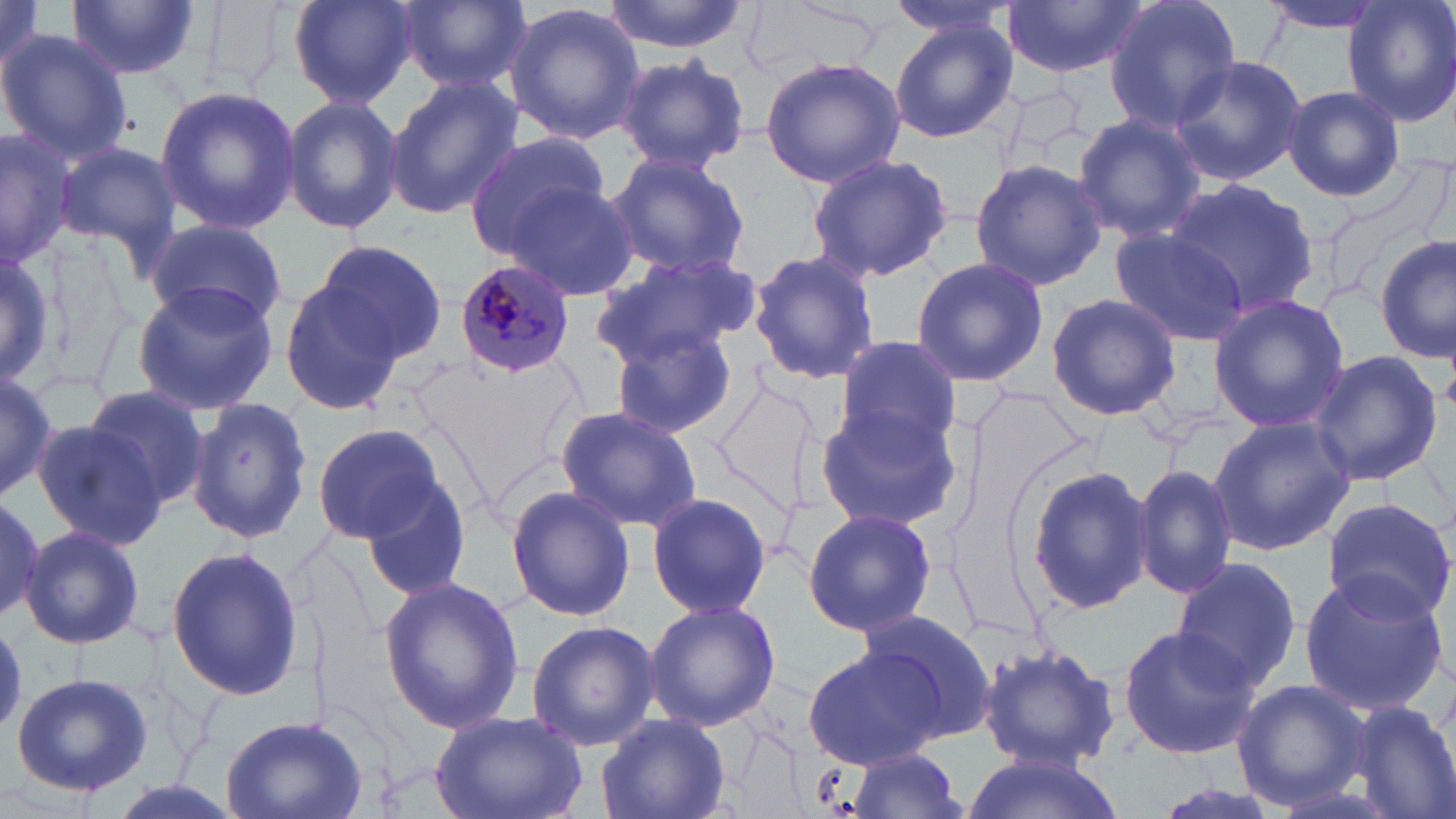 Approximate bounding boxes as named x1/y1/x2/y2 corners in pixels. Uninfected red blood cell locations: (x1=287, y1=0, x2=417, y2=107), (x1=396, y1=0, x2=529, y2=93), (x1=604, y1=0, x2=746, y2=54), (x1=883, y1=0, x2=1022, y2=40), (x1=1102, y1=0, x2=1242, y2=135), (x1=1262, y1=0, x2=1389, y2=39), (x1=1345, y1=0, x2=1456, y2=127), (x1=0, y1=1, x2=52, y2=93), (x1=68, y1=2, x2=197, y2=83), (x1=1003, y1=2, x2=1146, y2=81), (x1=502, y1=3, x2=645, y2=144), (x1=888, y1=22, x2=1018, y2=143), (x1=0, y1=27, x2=133, y2=164), (x1=617, y1=53, x2=748, y2=175), (x1=1168, y1=53, x2=1306, y2=185), (x1=759, y1=56, x2=906, y2=189), (x1=383, y1=76, x2=522, y2=219), (x1=153, y1=84, x2=301, y2=233), (x1=1282, y1=85, x2=1403, y2=204), (x1=282, y1=94, x2=403, y2=235), (x1=1072, y1=111, x2=1207, y2=247), (x1=0, y1=125, x2=79, y2=268), (x1=464, y1=130, x2=611, y2=263), (x1=56, y1=141, x2=182, y2=264), (x1=604, y1=150, x2=753, y2=282), (x1=805, y1=153, x2=953, y2=282), (x1=969, y1=159, x2=1108, y2=290), (x1=1165, y1=178, x2=1320, y2=319), (x1=503, y1=179, x2=639, y2=303), (x1=1343, y1=187, x2=1456, y2=343), (x1=145, y1=220, x2=288, y2=332), (x1=1108, y1=228, x2=1250, y2=345), (x1=1376, y1=238, x2=1455, y2=361), (x1=0, y1=239, x2=60, y2=394), (x1=310, y1=240, x2=445, y2=365), (x1=749, y1=249, x2=880, y2=385), (x1=593, y1=253, x2=761, y2=368), (x1=909, y1=255, x2=1049, y2=388), (x1=277, y1=275, x2=405, y2=416), (x1=132, y1=277, x2=280, y2=414), (x1=1046, y1=294, x2=1181, y2=422), (x1=1208, y1=296, x2=1350, y2=432), (x1=608, y1=325, x2=742, y2=440), (x1=834, y1=335, x2=961, y2=450), (x1=1306, y1=349, x2=1443, y2=486), (x1=0, y1=368, x2=56, y2=503), (x1=708, y1=370, x2=829, y2=533), (x1=80, y1=384, x2=212, y2=512), (x1=186, y1=395, x2=314, y2=546), (x1=814, y1=399, x2=962, y2=532), (x1=553, y1=405, x2=702, y2=533), (x1=1207, y1=415, x2=1355, y2=556), (x1=29, y1=417, x2=166, y2=549), (x1=313, y1=423, x2=445, y2=542), (x1=355, y1=461, x2=474, y2=605), (x1=1133, y1=462, x2=1239, y2=601), (x1=1024, y1=465, x2=1154, y2=613), (x1=505, y1=486, x2=636, y2=620), (x1=0, y1=493, x2=46, y2=626), (x1=648, y1=493, x2=771, y2=619), (x1=1322, y1=498, x2=1456, y2=626), (x1=801, y1=507, x2=938, y2=637), (x1=21, y1=524, x2=146, y2=650), (x1=165, y1=546, x2=303, y2=700), (x1=1172, y1=556, x2=1306, y2=693), (x1=1296, y1=570, x2=1450, y2=716), (x1=377, y1=576, x2=524, y2=735), (x1=645, y1=599, x2=780, y2=730), (x1=859, y1=609, x2=997, y2=742), (x1=525, y1=620, x2=660, y2=753), (x1=1116, y1=624, x2=1261, y2=759), (x1=805, y1=644, x2=949, y2=769), (x1=976, y1=644, x2=1120, y2=772), (x1=11, y1=671, x2=153, y2=798), (x1=1231, y1=679, x2=1371, y2=811), (x1=1344, y1=699, x2=1456, y2=819), (x1=430, y1=709, x2=590, y2=819), (x1=595, y1=713, x2=731, y2=819), (x1=218, y1=715, x2=369, y2=818), (x1=844, y1=747, x2=970, y2=819), (x1=960, y1=751, x2=1128, y2=819). Plasmodium malariae-infected red blood cell locations: (x1=455, y1=258, x2=577, y2=379). Slide-level diagnosis: Plasmodium malariae. Thin blood film. One field of a larger specimen. 1000x magnification. Image is 1456×819 pixels. May-Grünwald-Giemsa-stained preparation. Optical microscopy.